Describe the morphology of the red blood cells.
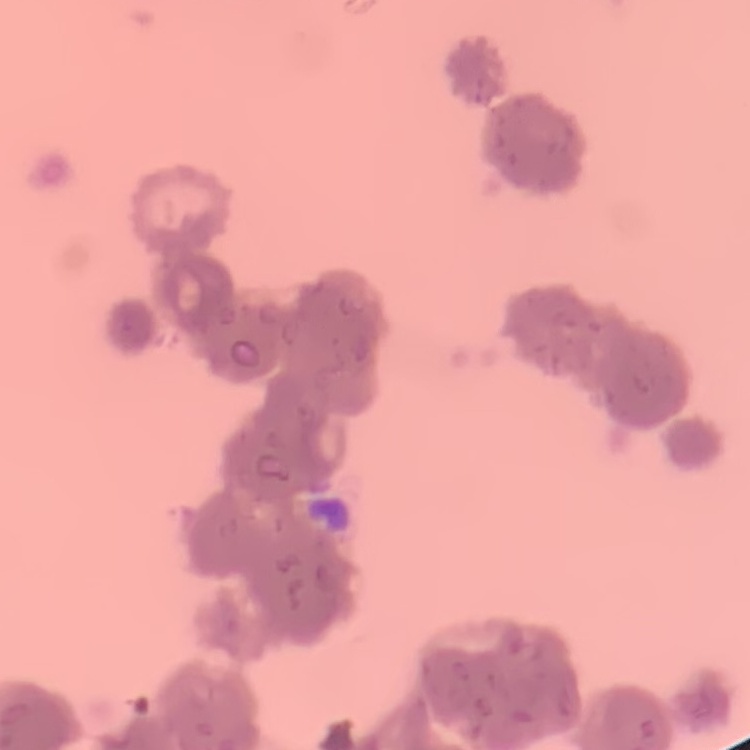
They show rouleaux formation.

Summary:
  - Preparation: thin peripheral smear
  - Image type: one tile cut from a larger photomicrograph
  - Stain: Field's or Giemsa